Report the malaria status of this cell.
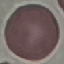

It is uninfected.

capture: smartphone through the microscope eyepiece
stain: Giemsa
image_type: automatically extracted cell patch, resized to 64 × 64 pixels
preparation: thin blood film